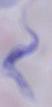

Summary:
  - Identification: trypanosome
  - Modality: photomicrograph
  - Magnification: 1000x